Point out each malaria parasite.
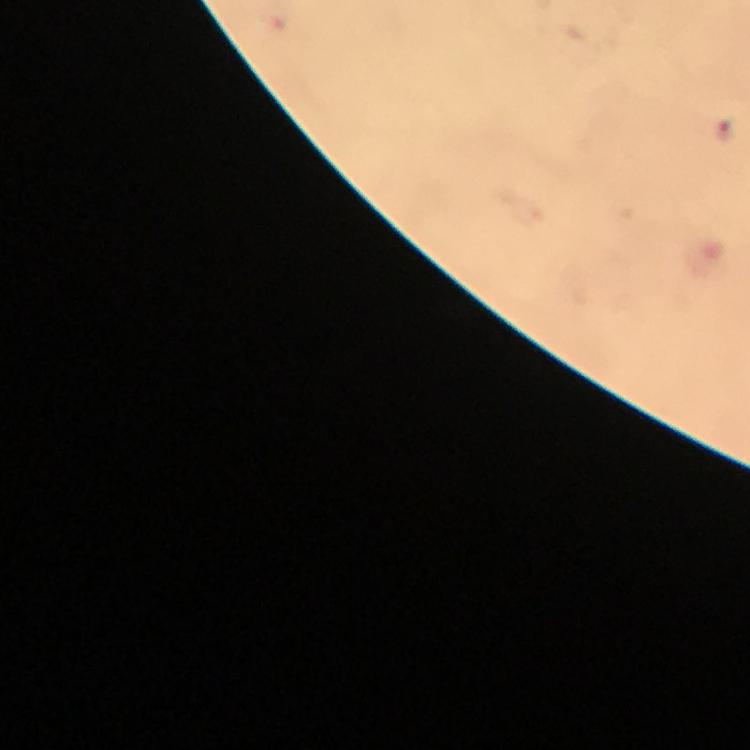

Approximate centers as [x, y] in pixels.
Malaria parasites: [726, 131].

preparation: thick smear
cropped_from: a single field of view
immersion_oil: used
context: from a diagnostic examination for malaria
image_size: 750×750 pixels
capture: smartphone mounted on the microscope
stain: Giemsa
magnification: 100x